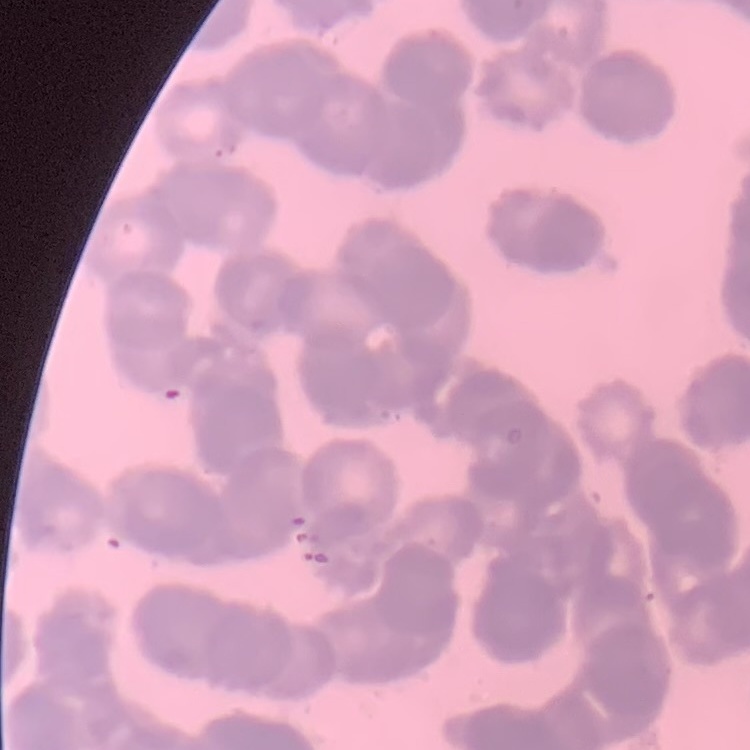

Summary:
  - Red blood cell morphology: rouleaux formation
  - Preparation: thin blood film
  - Stain: Field's or Giemsa
  - Image type: one tile cut from a larger photomicrograph